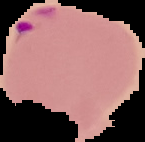
preparation = thin blood film
image size = 145×142 pixels
image type = segmented cell region with the area outside set to black
result = Plasmodium parasites detected